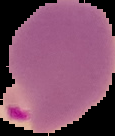

From a thin blood smear. Image is 115×136 pixels. Cell region segmented out of the field of view; the surrounding area is masked to black. Result: Plasmodium parasites identified.